Find each parasitized red blood cell.
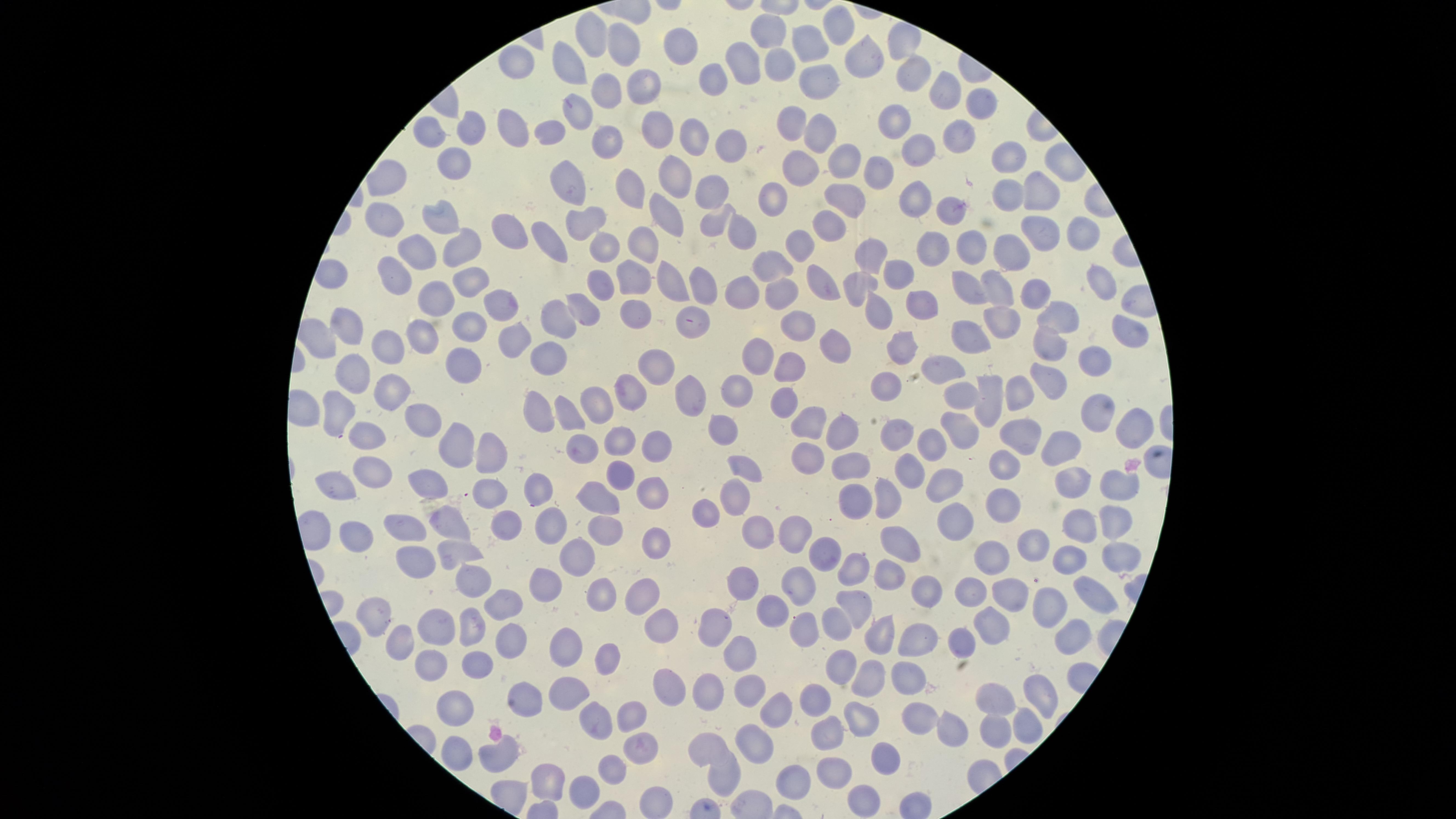

No parasitized red blood cells identified.

Approximate marker points, in pixels from the top-left corner. Uninfected red blood cells: (x=772, y=31), (x=839, y=31), (x=595, y=33), (x=684, y=45), (x=812, y=47), (x=629, y=50), (x=866, y=58), (x=749, y=59), (x=783, y=62), (x=516, y=64), (x=571, y=65), (x=909, y=72), (x=716, y=75), (x=646, y=81), (x=819, y=84), (x=943, y=90), (x=605, y=94), (x=981, y=106), (x=580, y=114), (x=897, y=120), (x=796, y=126), (x=428, y=129), (x=471, y=129), (x=513, y=129), (x=656, y=129), (x=550, y=131), (x=693, y=134), (x=820, y=134), (x=957, y=135), (x=608, y=139), (x=729, y=146), (x=916, y=150), (x=454, y=157), (x=851, y=158), (x=1016, y=160), (x=802, y=167), (x=882, y=168), (x=671, y=174), (x=571, y=176), (x=389, y=178), (x=624, y=185), (x=710, y=187), (x=847, y=194), (x=1040, y=194), (x=1010, y=195), (x=779, y=198), (x=916, y=201), (x=950, y=210), (x=662, y=211), (x=444, y=218), (x=588, y=218), (x=382, y=219), (x=711, y=222), (x=830, y=222), (x=745, y=229), (x=1043, y=229), (x=510, y=231), (x=1080, y=235), (x=544, y=239), (x=801, y=241), (x=977, y=242), (x=936, y=244), (x=1011, y=245), (x=417, y=247), (x=646, y=247), (x=464, y=249), (x=605, y=249), (x=880, y=250), (x=776, y=263), (x=902, y=273), (x=633, y=275), (x=815, y=275), (x=391, y=276), (x=1102, y=277), (x=671, y=279), (x=468, y=281), (x=704, y=282), (x=599, y=283), (x=864, y=283), (x=743, y=286), (x=970, y=287), (x=1001, y=287), (x=777, y=292), (x=1029, y=295), (x=436, y=302), (x=499, y=302), (x=924, y=306), (x=584, y=307), (x=631, y=308), (x=880, y=309), (x=1061, y=311), (x=557, y=316), (x=1012, y=318), (x=692, y=320), (x=463, y=324), (x=798, y=324), (x=345, y=325), (x=1134, y=329), (x=971, y=331), (x=512, y=333), (x=416, y=338), (x=833, y=340), (x=1053, y=340), (x=386, y=346), (x=901, y=346), (x=544, y=355), (x=758, y=356), (x=1097, y=360), (x=461, y=362), (x=947, y=365), (x=656, y=366), (x=353, y=368), (x=786, y=369), (x=888, y=382), (x=388, y=383), (x=1051, y=383), (x=738, y=388), (x=693, y=391), (x=991, y=391), (x=628, y=393), (x=1020, y=393), (x=783, y=396), (x=961, y=396), (x=595, y=404), (x=340, y=407), (x=1099, y=407), (x=539, y=409), (x=568, y=412), (x=420, y=415), (x=808, y=422), (x=1138, y=423), (x=721, y=424), (x=957, y=424), (x=840, y=425), (x=1019, y=435), (x=892, y=436), (x=619, y=440), (x=368, y=442), (x=1054, y=442), (x=457, y=444), (x=657, y=447), (x=933, y=448), (x=582, y=450), (x=491, y=458), (x=807, y=459), (x=854, y=464), (x=1007, y=465), (x=747, y=467), (x=910, y=471), (x=368, y=473), (x=617, y=477), (x=1076, y=477), (x=420, y=478), (x=340, y=484), (x=943, y=484), (x=1112, y=487), (x=645, y=490), (x=537, y=492), (x=491, y=494), (x=997, y=495), (x=597, y=498), (x=732, y=499), (x=888, y=499), (x=851, y=503), (x=704, y=508), (x=952, y=518), (x=547, y=519), (x=448, y=521), (x=1114, y=521), (x=604, y=523), (x=502, y=525), (x=399, y=528), (x=1083, y=530), (x=754, y=531), (x=795, y=536), (x=1029, y=538), (x=356, y=539), (x=653, y=541), (x=905, y=543), (x=823, y=550), (x=582, y=554), (x=1063, y=554), (x=459, y=556), (x=408, y=557), (x=993, y=557), (x=1117, y=557), (x=847, y=569), (x=881, y=576), (x=744, y=578), (x=471, y=580), (x=544, y=583), (x=795, y=587), (x=927, y=587), (x=972, y=589), (x=604, y=591), (x=641, y=594), (x=1093, y=595), (x=1006, y=597), (x=498, y=601), (x=767, y=605), (x=854, y=605), (x=1045, y=608), (x=378, y=616), (x=657, y=620), (x=835, y=620), (x=719, y=623), (x=991, y=624), (x=803, y=625), (x=432, y=628), (x=473, y=628), (x=885, y=635), (x=962, y=636), (x=1067, y=636), (x=920, y=642), (x=504, y=643), (x=398, y=644), (x=569, y=649), (x=735, y=650), (x=605, y=653), (x=426, y=662), (x=480, y=664), (x=837, y=671), (x=872, y=677), (x=906, y=678), (x=563, y=687), (x=675, y=687), (x=746, y=687), (x=711, y=690), (x=1041, y=694), (x=531, y=697), (x=1000, y=699), (x=816, y=700), (x=451, y=704), (x=774, y=707), (x=860, y=716), (x=591, y=717), (x=635, y=717), (x=919, y=717), (x=1026, y=724), (x=952, y=726), (x=994, y=728), (x=828, y=732), (x=708, y=742), (x=755, y=742), (x=453, y=750), (x=636, y=750), (x=501, y=753), (x=889, y=758), (x=608, y=767), (x=834, y=770), (x=550, y=772), (x=721, y=774), (x=790, y=779), (x=584, y=786), (x=866, y=797). Single field of view. Image is 1456×819 pixels. Thin blood film. Smartphone photograph through the microscope eyepiece. Giemsa-stained preparation. Circular visible region.